Assess the morphology of the red blood cells.
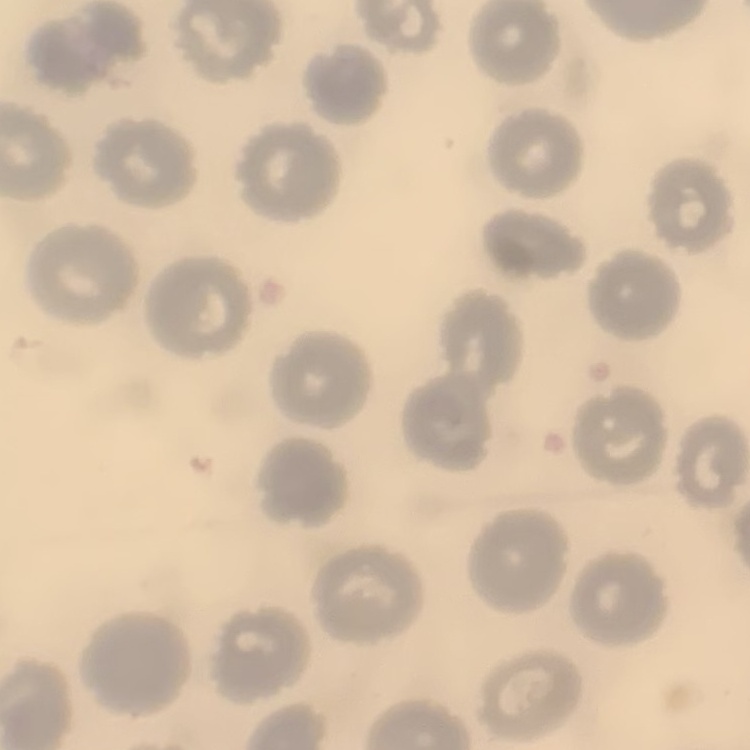
They show no rouleaux formation.

Field's or Giemsa stain. Thin blood film. Square crop of a larger photomicrograph.